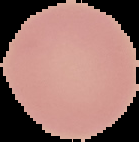 Image is 139×142 pixels. Malaria status: uninfected. From a thin blood film. The area outside the segmented cell region is set to black.